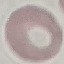

Summary:
  - Malaria status: uninfected
  - Image type: automatically extracted cell patch, resized to 64 × 64 pixels
  - Stain: Giemsa
  - Capture: smartphone through the microscope eyepiece
  - Preparation: thin blood film